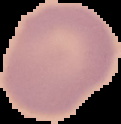

result = negative for malaria parasites
image type = cell region segmented out of the field of view; surrounding area masked to black
image size = 121×124 pixels
preparation = thin blood film